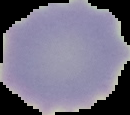
The area outside the segmented cell region is set to black. From a thin blood film. Malaria status: uninfected. Image is 130×115 pixels.